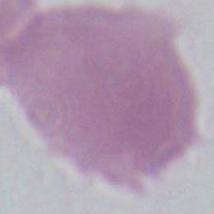

Micrograph. An erythrocyte is seen. 1000x magnification.